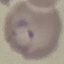
Malaria status: parasitized. Thin smear of blood. Automatically extracted cell patch, resized to 64 × 64 pixels. Giemsa stain. Photographed with a smartphone camera at the microscope eyepiece.